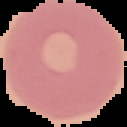

result: no malaria parasites detected
image_type: segmented cell region with the area outside set to black
image_size: 127×127 pixels
preparation: thin blood smear